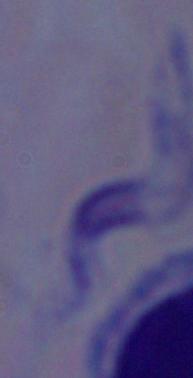
Summary:
  - Identification: trypanosome
  - Magnification: 1000x
  - Modality: photomicrograph